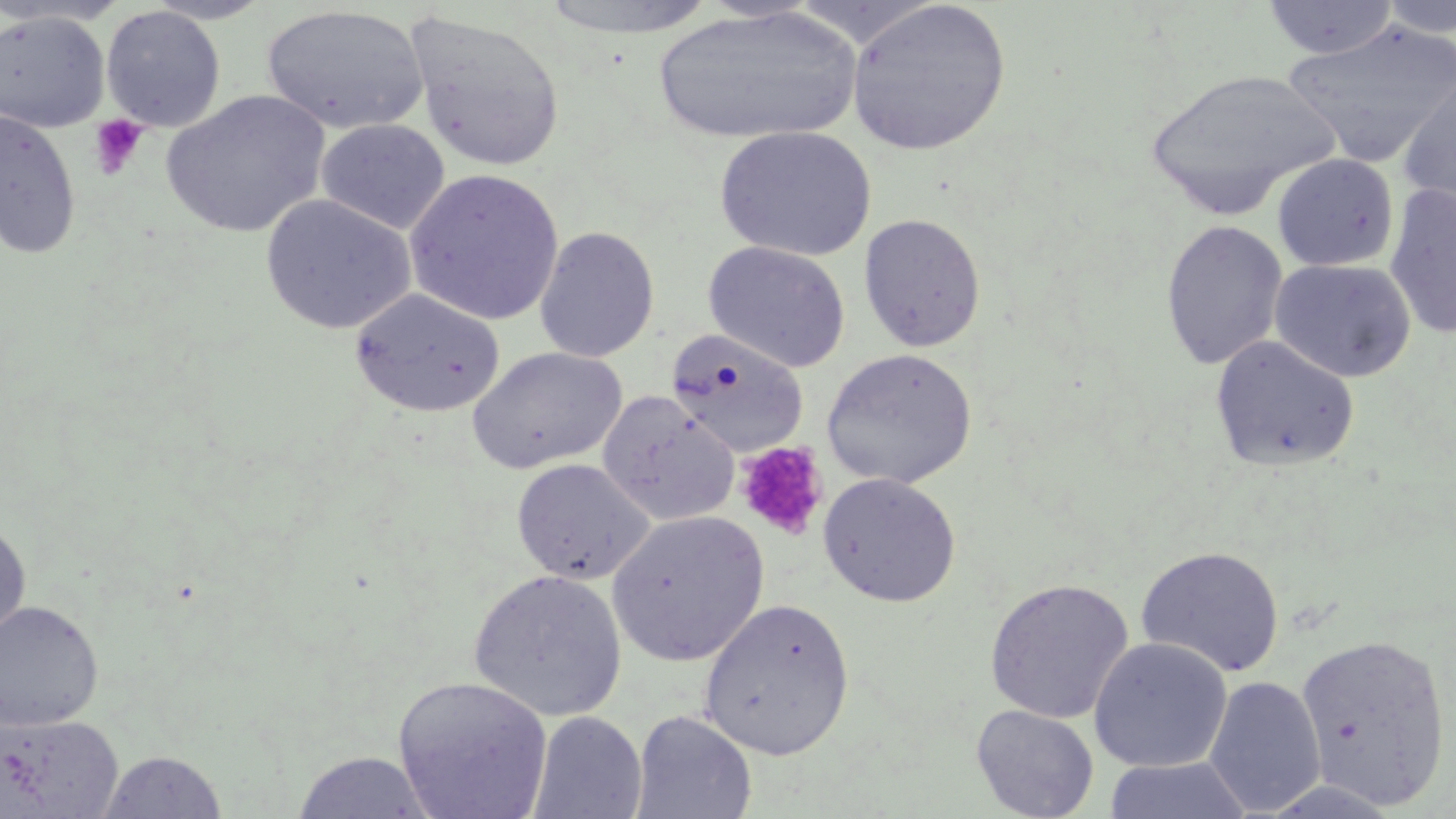
Approximate bounding boxes as named x1/y1/x2/y2 corners in pixels. Platelet locations: (x1=88, y1=115, x2=149, y2=181), (x1=735, y1=441, x2=829, y2=541). Uninfected red blood cell locations: (x1=143, y1=0, x2=275, y2=24), (x1=538, y1=0, x2=719, y2=40), (x1=845, y1=0, x2=1011, y2=156), (x1=1260, y1=0, x2=1400, y2=61), (x1=1377, y1=0, x2=1456, y2=41), (x1=0, y1=1, x2=130, y2=28), (x1=101, y1=5, x2=226, y2=132), (x1=262, y1=5, x2=429, y2=136), (x1=653, y1=5, x2=861, y2=148), (x1=0, y1=10, x2=111, y2=132), (x1=404, y1=10, x2=566, y2=172), (x1=1282, y1=20, x2=1455, y2=168), (x1=1145, y1=67, x2=1341, y2=220), (x1=1396, y1=71, x2=1456, y2=221), (x1=160, y1=89, x2=331, y2=238), (x1=0, y1=108, x2=82, y2=261), (x1=316, y1=119, x2=450, y2=234), (x1=714, y1=126, x2=877, y2=262), (x1=1271, y1=153, x2=1400, y2=272), (x1=405, y1=169, x2=565, y2=326), (x1=1383, y1=182, x2=1456, y2=339), (x1=260, y1=194, x2=417, y2=335), (x1=859, y1=213, x2=986, y2=352), (x1=1160, y1=219, x2=1288, y2=371), (x1=534, y1=226, x2=659, y2=363), (x1=703, y1=240, x2=851, y2=373), (x1=1269, y1=258, x2=1417, y2=383), (x1=349, y1=288, x2=505, y2=417), (x1=666, y1=329, x2=809, y2=456), (x1=1210, y1=334, x2=1361, y2=473), (x1=467, y1=346, x2=627, y2=474), (x1=821, y1=348, x2=977, y2=489), (x1=598, y1=392, x2=739, y2=525), (x1=511, y1=459, x2=654, y2=584), (x1=818, y1=472, x2=961, y2=607), (x1=607, y1=510, x2=768, y2=666), (x1=0, y1=519, x2=32, y2=645), (x1=1135, y1=545, x2=1286, y2=677), (x1=468, y1=568, x2=627, y2=722), (x1=984, y1=577, x2=1134, y2=723), (x1=698, y1=597, x2=855, y2=759), (x1=0, y1=599, x2=104, y2=732), (x1=1295, y1=630, x2=1453, y2=810), (x1=1088, y1=636, x2=1233, y2=773), (x1=392, y1=675, x2=553, y2=819), (x1=1204, y1=675, x2=1327, y2=815), (x1=971, y1=704, x2=1099, y2=819), (x1=630, y1=709, x2=757, y2=819), (x1=528, y1=710, x2=647, y2=819), (x1=1, y1=714, x2=123, y2=818), (x1=97, y1=749, x2=228, y2=818), (x1=290, y1=750, x2=438, y2=818), (x1=1102, y1=756, x2=1253, y2=818). Slide-level diagnosis: negative for blood parasites. Image is 1456×819 pixels. Single field of view. Thin blood film. 1000x magnification. Light microscopy. May-Grünwald-Giemsa stain.